Point out each malaria parasite.
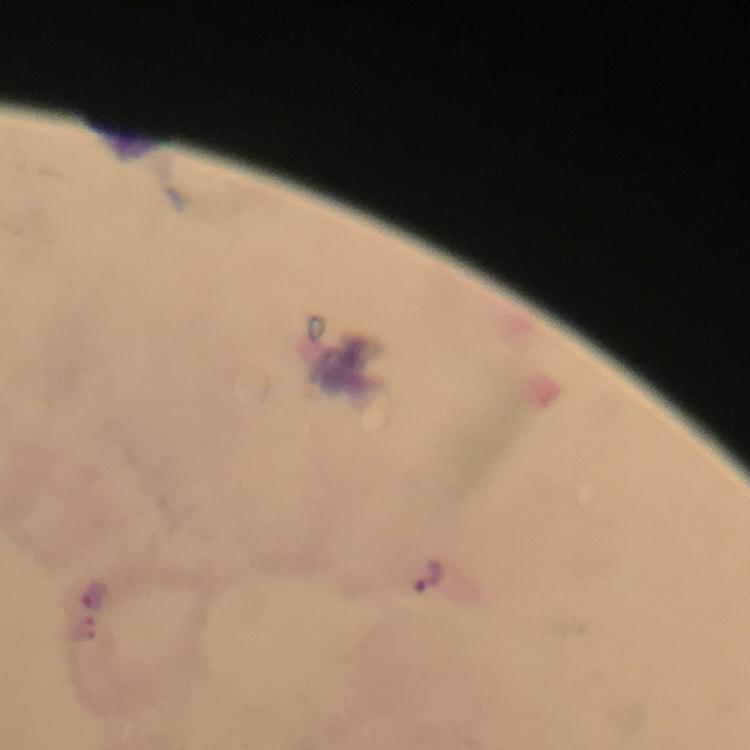
Approximate centers as {x, y} in pixels.
Malaria parasites: {427, 576}, {94, 592}.

Summary:
  - Context: from a malaria diagnostic workup
  - Immersion oil: used
  - Stain: Giemsa
  - Image size: 750×750 pixels
  - Magnification: 100x
  - Preparation: thick blood film
  - Cropped from: a single field of view
  - Capture: smartphone mounted on the microscope